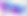

identification: Toxoplasma gondii
magnification: 400x
modality: photomicrograph